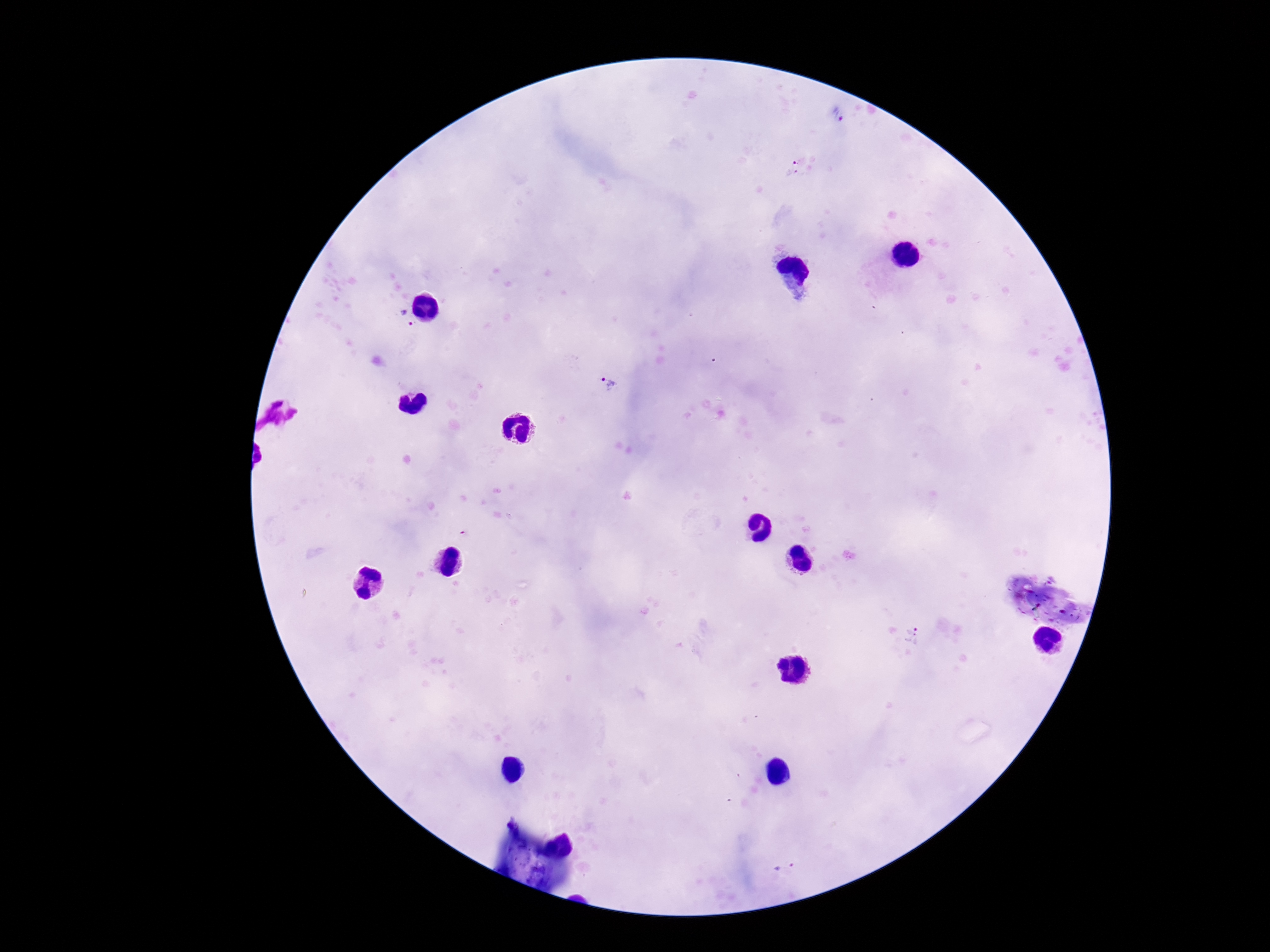

Approximate centers as (x, y) in pixels. Plasmodium parasite locations: (836, 117), (795, 168), (406, 319), (606, 384), (912, 636), (787, 868). Giemsa stain. One field from this slide. 100x magnification. Image is 1270×952 pixels. Patient malaria status: infected. Thick blood smear. Smartphone photograph taken through the microscope eyepiece.